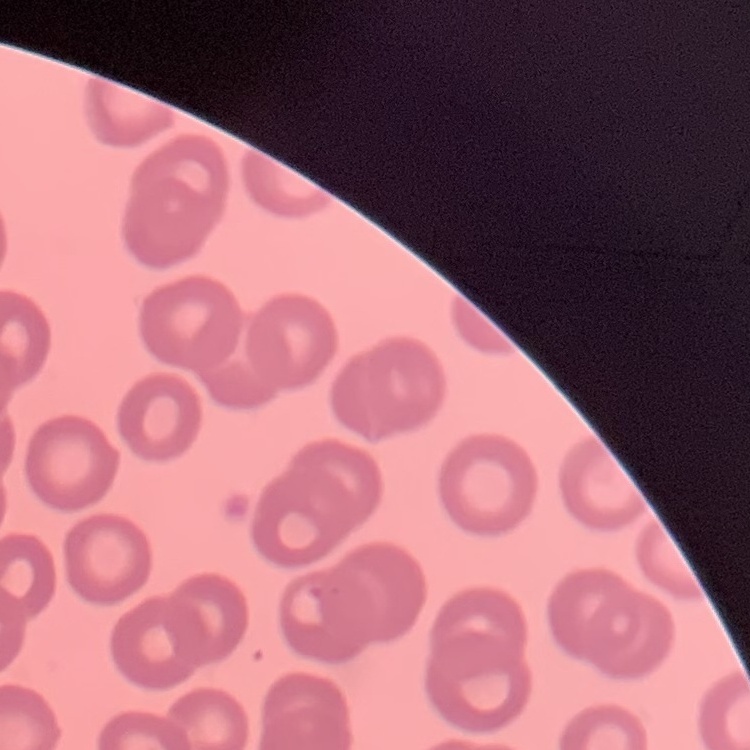

The erythrocytes show no rouleaux formation. Square crop of a larger photomicrograph. Thin blood smear. Field's or Giemsa stain.